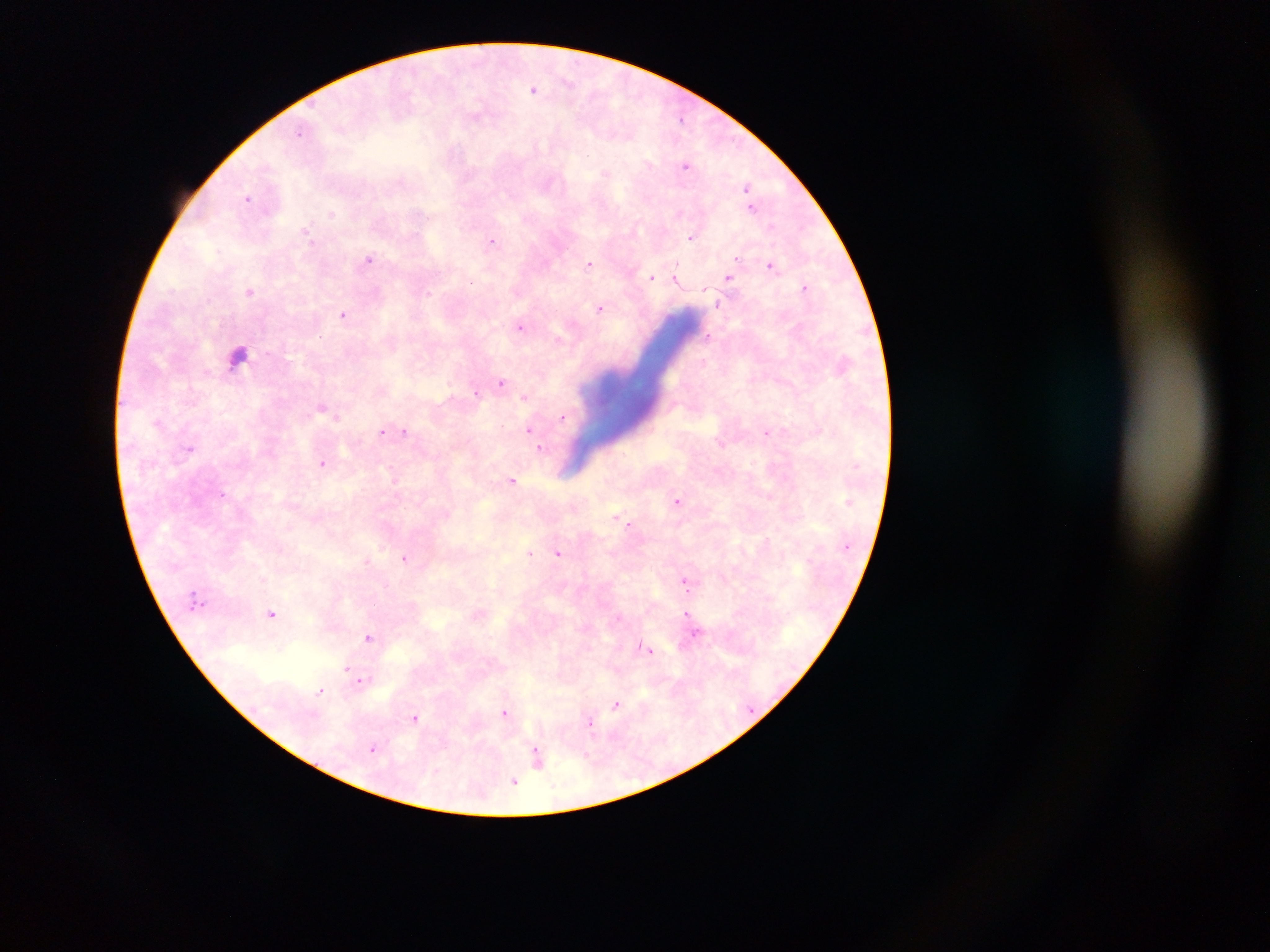
Approximate centers as x y in pixels.
Summary:
  - Leukocyte locations: 239 355
  - Malaria parasite locations: 534 89; 686 164; 606 172; 748 189; 248 198; 753 205; 307 232; 692 237; 492 241; 369 259; 590 263; 773 265; 677 275; 651 276; 729 277; 806 287; 250 291; 719 303; 601 308; 345 314; 521 326; 708 336; 559 339; 702 363; 502 382; 477 393; 526 397; 323 407; 562 415; 159 423; 529 430; 384 431; 403 432; 767 432; 191 447; 541 449; 322 463; 513 480; 678 502; 619 519; 630 524; 559 551; 530 553; 406 557; 369 560; 687 584; 272 613; 480 613; 689 614; 695 632; 370 636; 646 648; 346 668; 362 680; 322 690; 617 703; 505 712; 415 717; 591 722; 374 747; 538 756; 514 781
  - Field of view: single
  - Preparation: thick blood smear
  - Country: Ghana
  - Image size: 1270×952 pixels
  - Capture: mobile-phone photograph through a microscope